Outline each Plasmodium ovale-infected red blood cell.
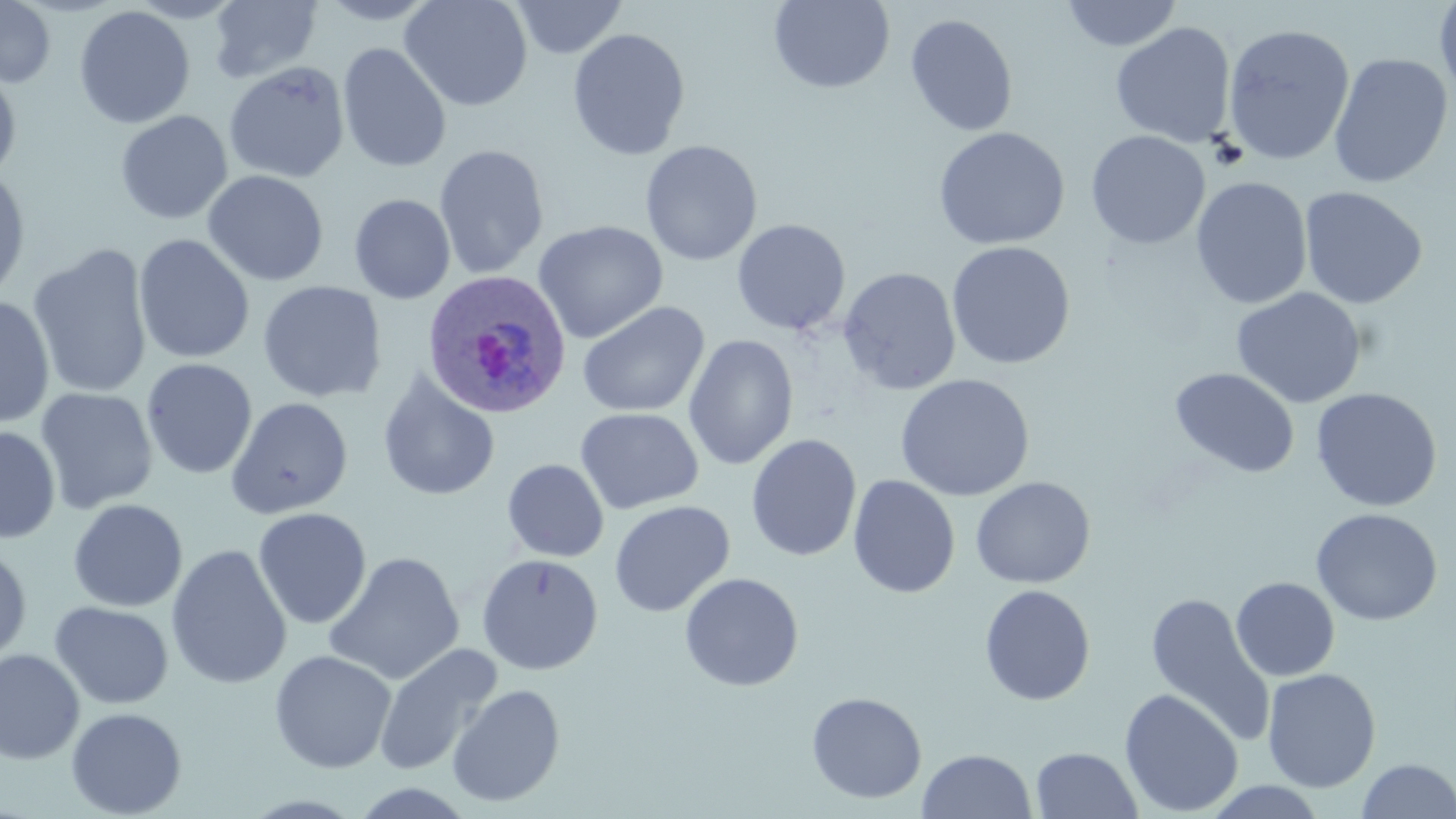

Approximate bounding boxes as (x1,y1)-(x2,y2) corner pairs in pixels.
Plasmodium ovale-infected red blood cells: (420,269)-(570,418).

slide_level_diagnosis: Plasmodium ovale
image_size: 1456×819 pixels
preparation: thin blood film
uninfected_red_blood_cell_locations: 'approximate bounding boxes as (x1,y1)-(x2,y2) corner pairs in pixels: (0,0)-(56,88), (313,0)-(443,25), (399,0)-(533,112), (510,0)-(628,58), (768,0)-(895,93), (1060,0)-(1183,52), (1434,0)-(1456,104), (207,1)-(323,85), (74,5)-(195,130), (905,13)-(1018,137), (1110,22)-(1236,148), (1221,24)-(1355,166), (567,28)-(691,161), (337,43)-(452,173), (1328,53)-(1453,190), (223,61)-(350,183), (0,66)-(22,183), (115,110)-(233,225), (932,126)-(1070,250), (1086,130)-(1210,249), (640,140)-(762,266), (433,144)-(549,279), (0,167)-(31,307), (203,170)-(329,287), (1190,177)-(1312,310), (1299,186)-(1427,309), (349,194)-(456,304), (732,219)-(851,336), (533,220)-(668,344), (133,234)-(255,365), (946,241)-(1075,369), (27,243)-(154,399), (838,267)-(961,395), (257,280)-(387,403), (1231,287)-(1367,409), (0,296)-(56,428), (577,301)-(710,417), (683,335)-(798,471), (140,358)-(258,480), (1169,367)-(1301,478), (377,370)-(500,502), (894,373)-(1035,501), (35,387)-(158,514), (1311,387)-(1443,512), (226,396)-(354,519), (574,407)-(703,515), (0,426)-(60,544), (746,434)-(862,561), (502,459)-(609,562), (848,475)-(960,598), (970,476)-(1096,589), (67,498)-(188,612), (609,500)-(735,617), (253,507)-(372,629), (1310,508)-(1443,626), (166,544)-(292,690), (0,546)-(32,667), (323,551)-(465,686), (476,553)-(604,675), (679,572)-(804,692), (1231,577)-(1340,681), (979,584)-(1096,706), (1145,592)-(1274,745), (50,601)-(174,709), (373,643)-(502,777), (0,649)-(85,764), (269,649)-(397,774), (1261,668)-(1382,792), (446,683)-(565,808), (1119,689)-(1244,816), (806,692)-(927,804), (66,706)-(187,818), (1031,747)-(1143,818), (917,749)-(1037,819), (1355,758)-(1455,818)'
field_of_view: single
magnification: 1000x
stain: May-Grünwald-Giemsa
modality: optical microscopy